Give the position of every leukocyte visible.
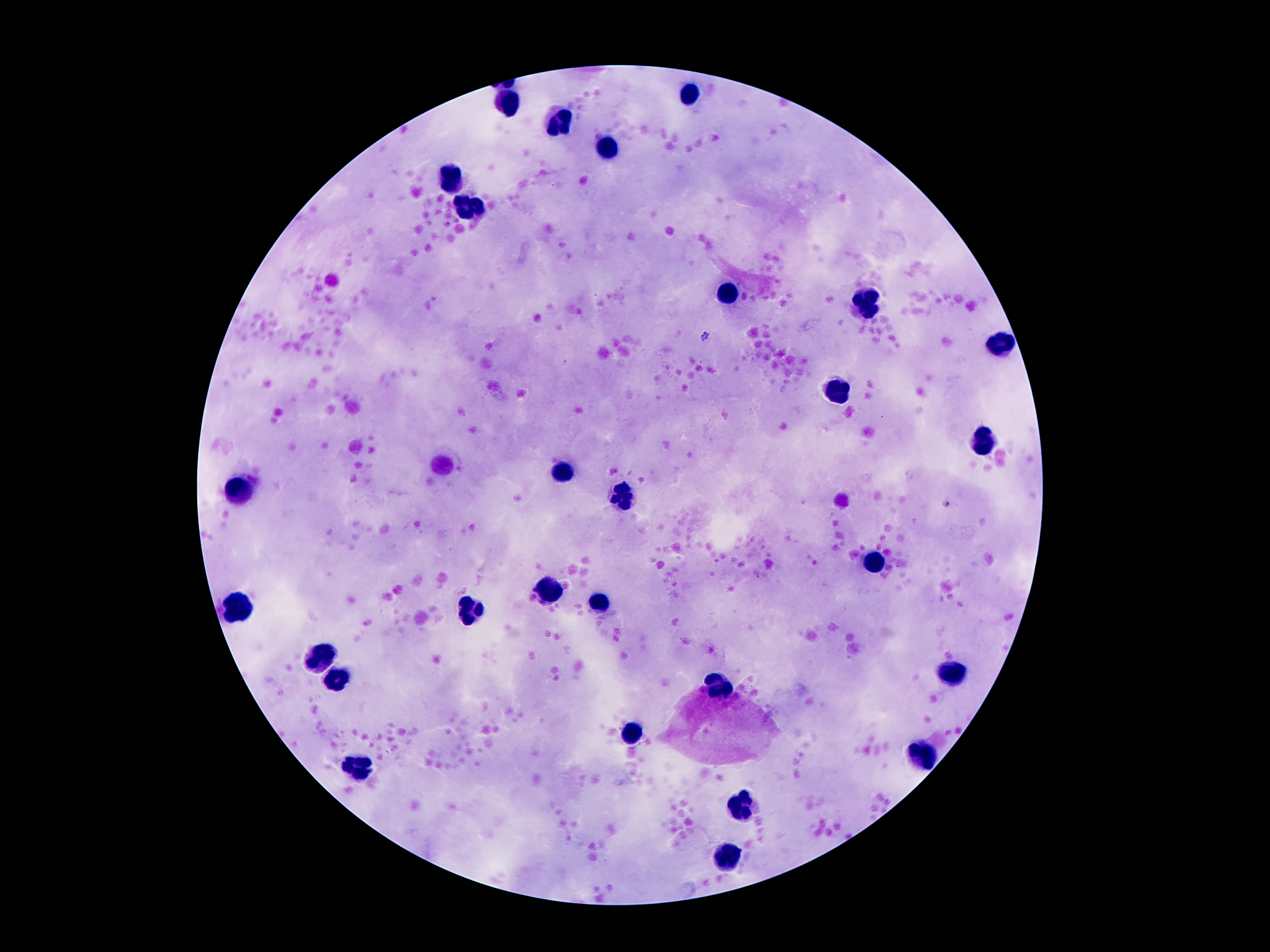
Approximate centers as {x, y} in pixels.
Leukocytes: {695, 93}, {509, 105}, {556, 122}, {613, 146}, {451, 174}, {476, 211}, {732, 291}, {865, 299}, {1002, 343}, {840, 391}, {986, 445}, {566, 472}, {242, 486}, {619, 492}, {879, 563}, {547, 591}, {238, 603}, {597, 606}, {470, 613}, {322, 652}, {953, 673}, {339, 681}, {721, 686}, {634, 732}, {924, 757}, {357, 766}, {744, 806}, {728, 858}.

image size = 1270×952 pixels
preparation = thick peripheral-blood smear
stain = Giemsa
magnification = 100x
capture = smartphone camera through the microscope eyepiece
field of view = single
patient malaria status = uninfected